Locate every Plasmodium parasite and identify its life-cycle stage.
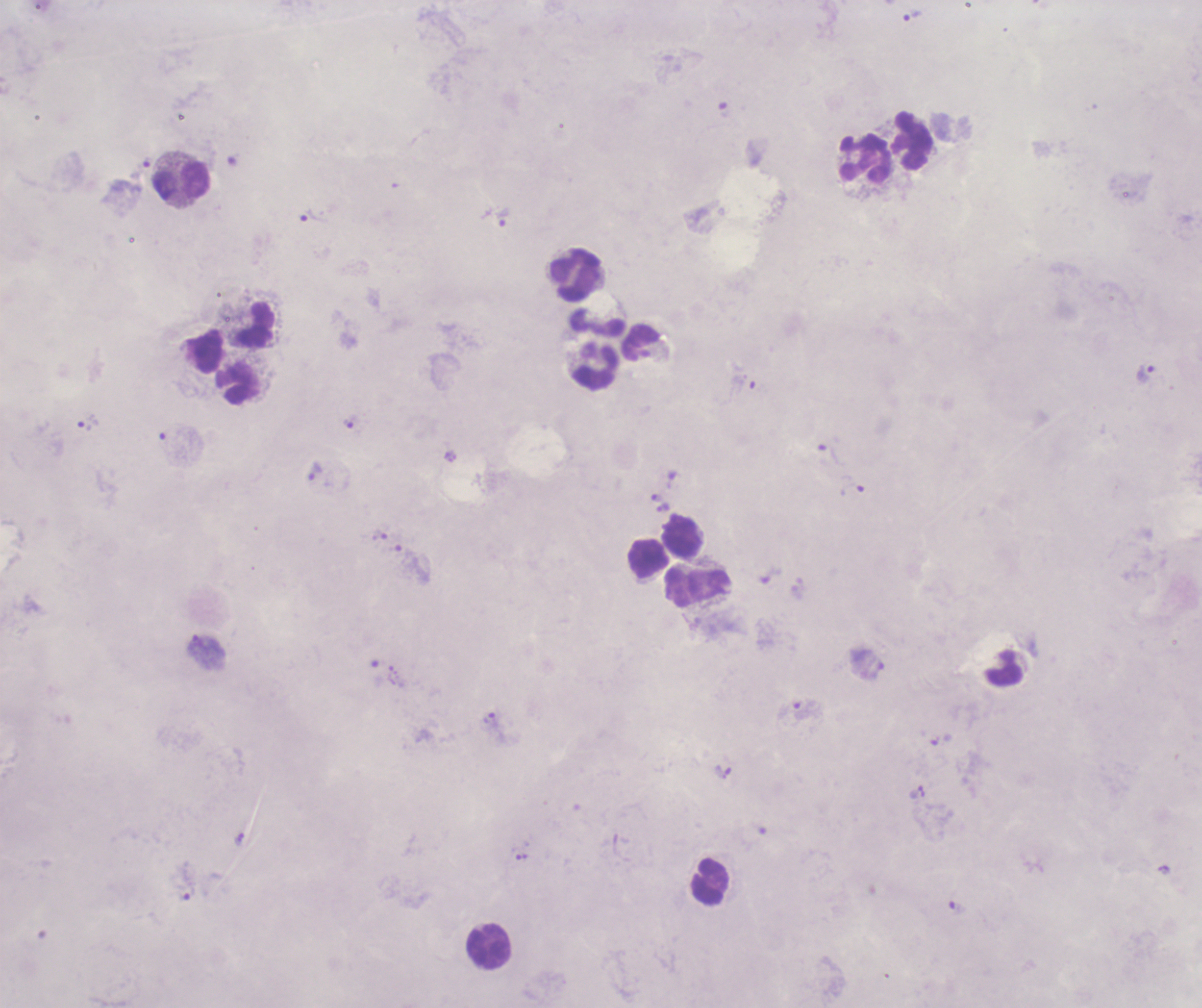
Approximate centers as [x, y] in pixels.
Trophozoites: [913, 16], [141, 167], [309, 216], [503, 219], [1147, 372], [744, 386], [350, 422], [87, 423], [828, 454], [314, 470], [852, 487], [656, 496], [663, 508], [379, 535], [205, 642], [877, 670], [804, 711], [490, 719], [724, 771], [521, 856], [189, 893], [958, 907].
No schizont or gametocyte forms observed.

coordinate format = approximate centers as [x, y] in pixels
leukocyte locations = [912, 140], [866, 160], [181, 181], [576, 276], [597, 321], [256, 324], [640, 342], [207, 351], [597, 368], [238, 384], [680, 535], [647, 556], [710, 583], [681, 587], [1005, 667], [710, 880], [489, 947]
background quality = unsatisfactory
stain = Romanowsky
context = previously used in a real diagnosis
field of view = single
magnification = 100x
coloration quality = bad
image size = 1202×1008 pixels
preparation = thick blood smear